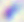 Captured at 400x magnification. Toxoplasma gondii is seen. Photomicrograph.